Give the position of every leukocyte visible.
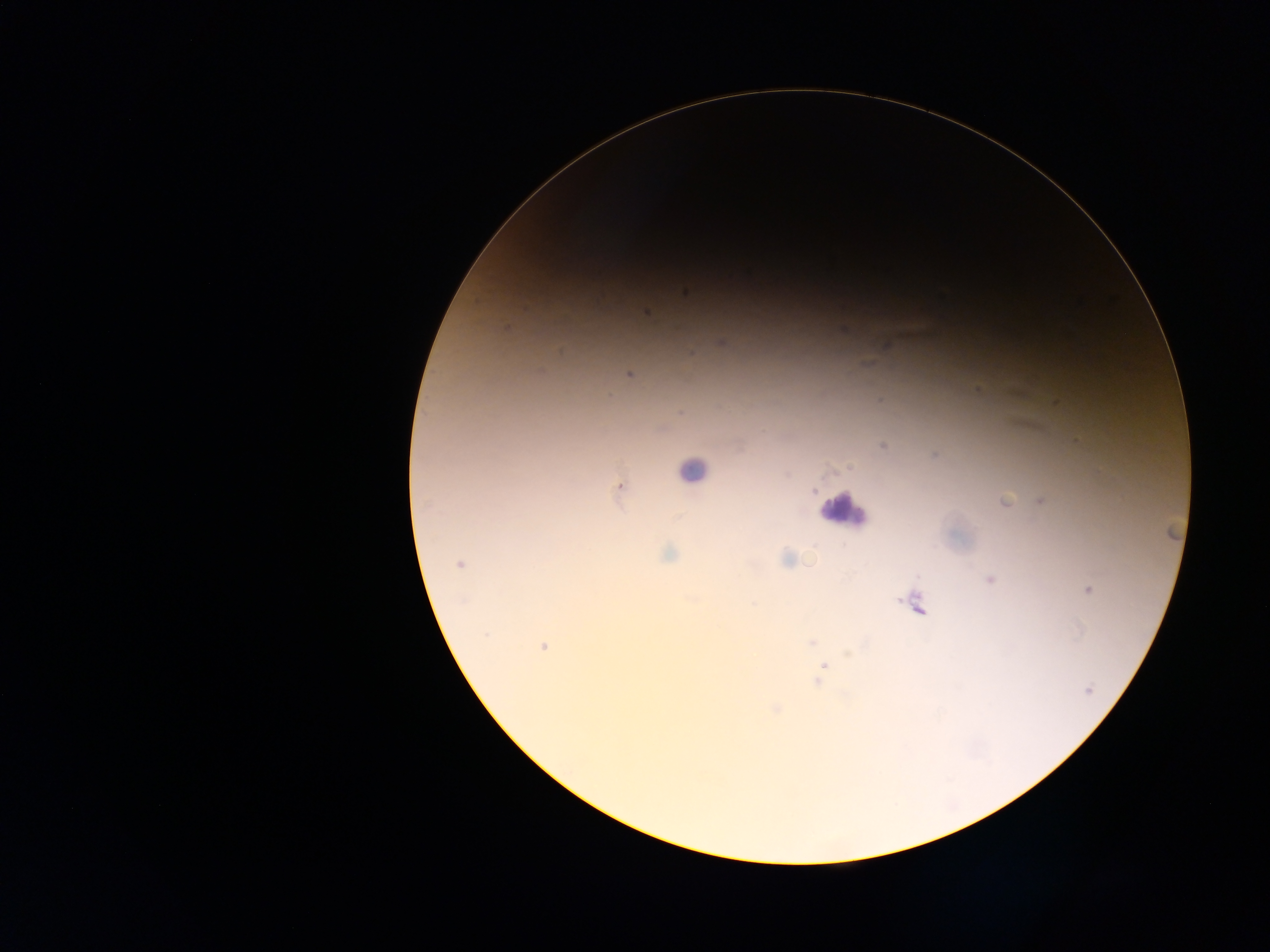
Approximate centers as [x, y] in pixels.
Leukocytes: [692, 470], [844, 509].

Plasmodium parasite locations: [646, 312], [720, 342], [629, 374], [880, 400], [682, 413], [882, 446], [935, 455], [619, 486], [1005, 500], [1041, 501], [669, 554], [787, 559], [460, 564], [989, 580], [1089, 589], [753, 604], [915, 604], [485, 635], [811, 642], [543, 647], [824, 667], [818, 681], [1089, 690], [776, 708]. Thick blood film. Collected in Ghana. Single field of view. Image is 1270×952 pixels. Photographed through a microscope with a mobile-phone camera.